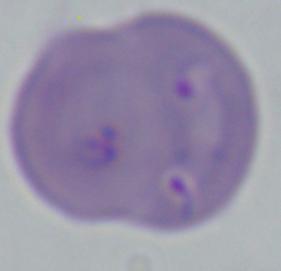

magnification: 1000x
modality: photomicrograph
identification: Babesia